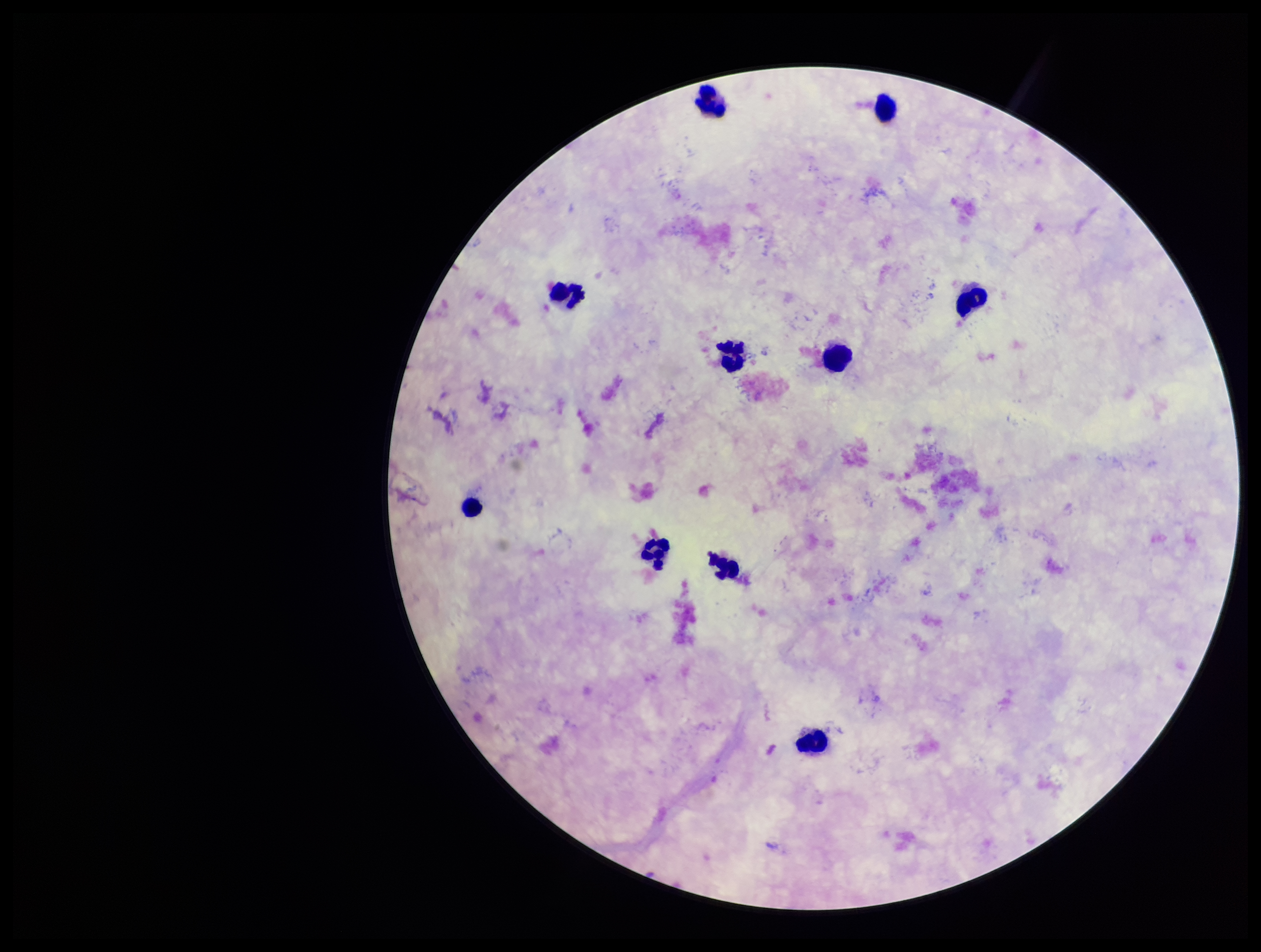 Giemsa stain. Parasite count: 0. Plasmodium parasites: none detected. Preparation: thick smear. Photographed through the microscope eyepiece with a smartphone camera. Leukocyte count: 10. Patient malaria status: negative. Single field of view. Image is 1261×952 pixels.